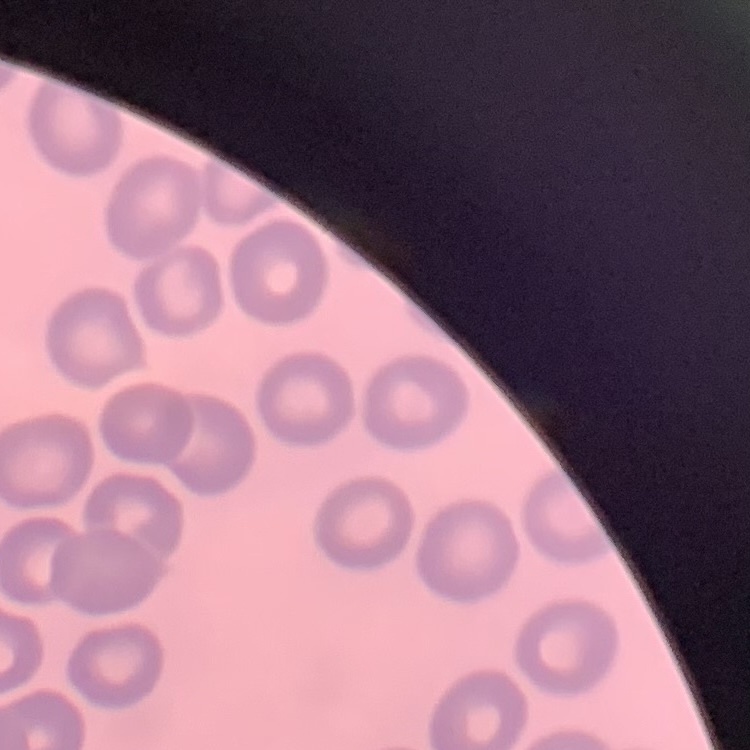
The red blood cells exhibit no rouleaux formation. Square crop of a larger photomicrograph. Stained with either Field's or Giemsa. Thin blood film.